State which parasite is depicted.
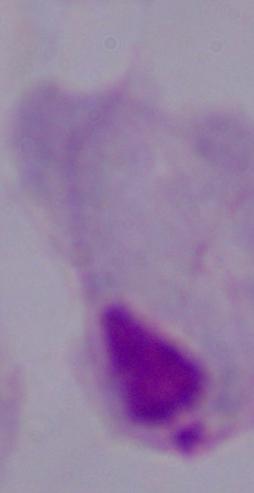
This is a trichomonad.

1000x magnification. Photomicrograph.